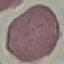

Summary:
  - Malaria status: uninfected
  - Stain: Giemsa
  - Capture: smartphone camera at the microscope eyepiece
  - Preparation: thin smear
  - Image type: automatically extracted cell patch, resized to 64 × 64 pixels